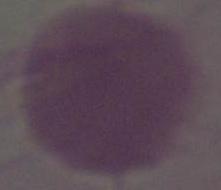

Photomicrograph. A red blood cell is shown. Captured at 1000x magnification.